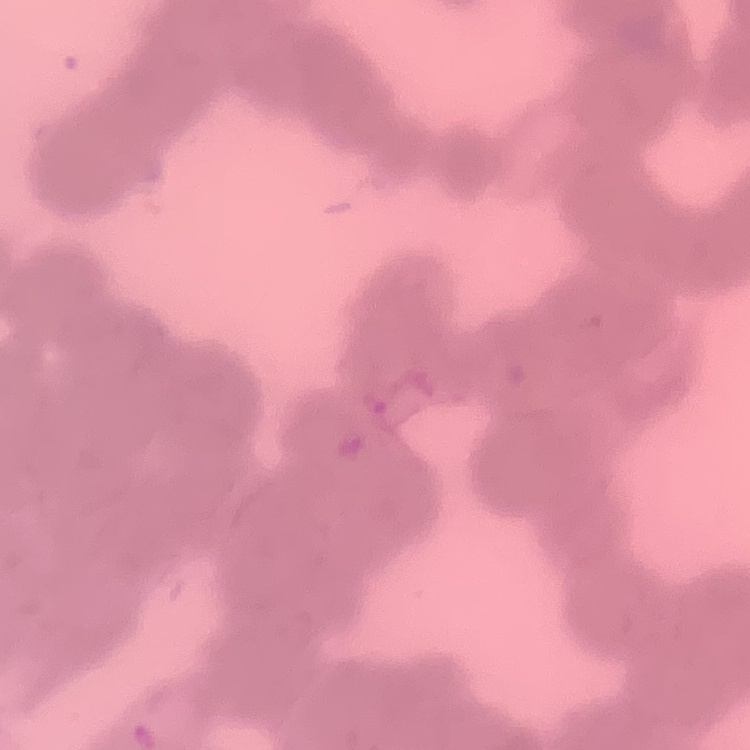
Summary:
  - Erythrocyte morphology: rouleaux formation
  - Stain: Field's or Giemsa
  - Preparation: thin blood smear
  - Image type: square crop of a larger photomicrograph